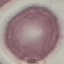
{
  "result": "negative for malaria parasites",
  "preparation": "thin blood smear",
  "stain": "Giemsa",
  "capture": "smartphone camera at the microscope eyepiece",
  "image_type": "automatically extracted cell patch, resized to 64 × 64 pixels"
}